Classify this cell by malaria status.
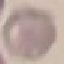
Uninfected.

Thin blood smear. Cell patch, automatically extracted from a larger field of view and resized to 64 × 64 pixels. Giemsa stain. Acquired by smartphone through the microscope eyepiece.